Outline each blood parasite and name the species.
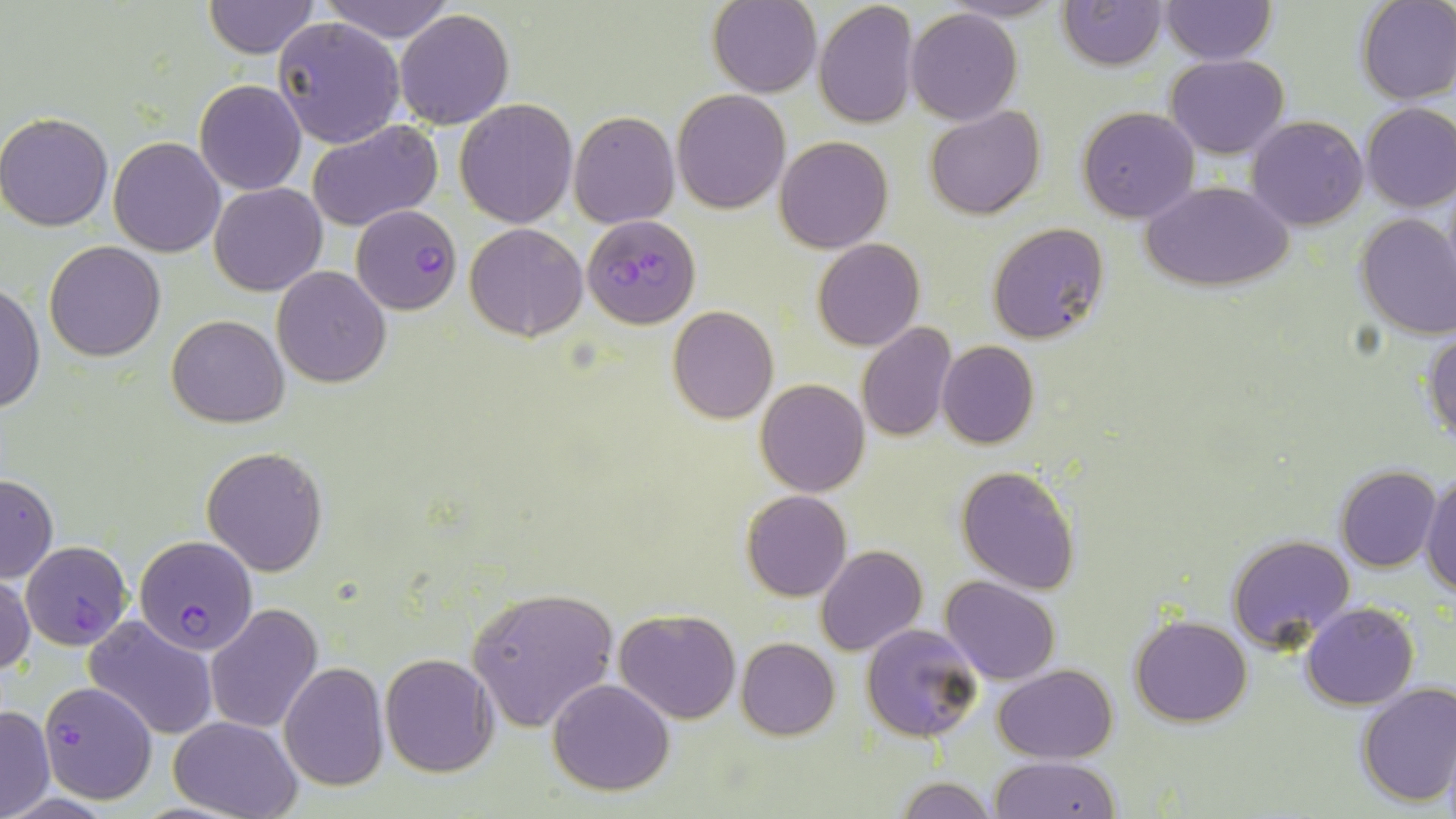

Approximate bounding boxes as (x1,y1)-(x2,y2) corner pairs in pixels.
Plasmodium falciparum-infected red blood cells: (352,204)-(460,315), (583,215)-(700,329), (133,534)-(257,654), (21,541)-(132,648), (38,680)-(157,805).
No Plasmodium ovale, Plasmodium malariae, Plasmodium vivax, Babesia divergens, or Trypanosoma brucei observed.

Summary:
  - Uninfected red blood cell locations: (708,0)-(820,97), (1057,0)-(1167,70), (1159,0)-(1275,64), (1356,0)-(1456,104), (201,1)-(320,58), (317,1)-(458,42), (813,1)-(918,131), (905,7)-(1023,126), (393,8)-(514,129), (271,16)-(405,148), (1166,54)-(1288,159), (194,79)-(307,196), (671,89)-(791,214), (455,98)-(577,228), (1362,104)-(1456,213), (925,106)-(1045,220), (1077,106)-(1198,222), (0,111)-(115,232), (570,111)-(679,227), (1246,116)-(1368,231), (306,121)-(442,231), (109,136)-(226,256), (775,136)-(892,254), (1144,180)-(1293,292), (210,182)-(327,296), (1355,212)-(1456,338), (989,222)-(1109,346), (465,223)-(587,341), (44,241)-(166,362), (812,241)-(923,350), (272,266)-(391,387), (1,280)-(43,417), (667,305)-(778,424), (166,315)-(290,427), (856,322)-(956,442), (1424,329)-(1456,444), (937,341)-(1037,449), (756,379)-(869,496), (202,447)-(328,576), (956,465)-(1079,595), (1336,465)-(1441,571), (1421,468)-(1456,596), (0,474)-(58,585), (742,490)-(851,602), (1226,533)-(1356,653), (817,546)-(926,657), (0,572)-(35,677), (941,575)-(1060,684), (467,587)-(620,732), (1302,602)-(1418,709), (205,604)-(322,735), (614,608)-(741,725), (1132,614)-(1252,727), (83,616)-(219,742), (861,623)-(983,742), (736,637)-(839,739), (380,653)-(499,777), (278,662)-(390,792), (993,665)-(1118,763), (547,678)-(676,796), (1355,681)-(1456,808), (0,703)-(53,819), (169,716)-(302,819), (1440,743)-(1456,819), (991,756)-(1120,818), (894,777)-(999,818)
  - Slide-level diagnosis: Plasmodium falciparum
  - Stain: May-Grünwald-Giemsa
  - Image size: 1456×819 pixels
  - Field of view: one of a larger specimen
  - Magnification: 1000x
  - Preparation: thin blood film
  - Modality: light microscopy